Comment on the morphology of the red blood cells.
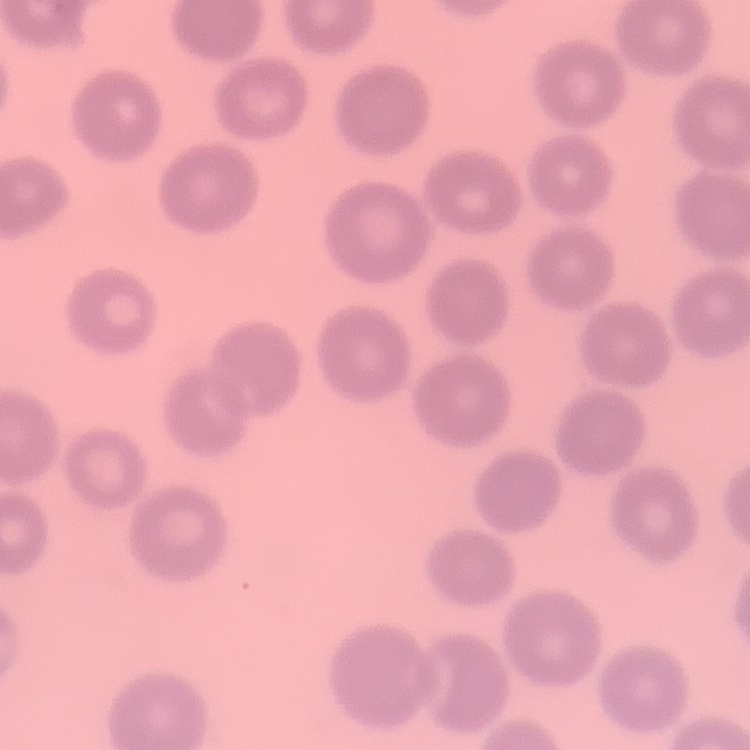
No rouleaux formation.

Stained with either Field's or Giemsa. Square crop of a larger photomicrograph. Thin blood film.